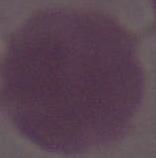
{
  "magnification": "1000x",
  "identification": "erythrocyte",
  "modality": "photomicrograph"
}